Describe the morphology of the red blood cells.
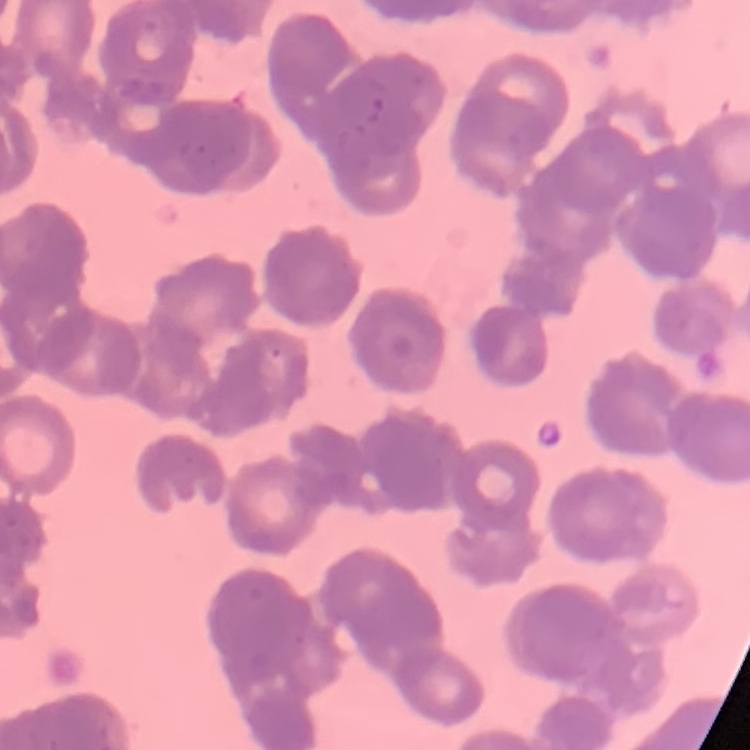

Rouleaux formation.

stain = Field's or Giemsa
preparation = thin blood smear
image type = one tile cut from a larger photomicrograph